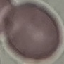
result: negative for malaria parasites
stain: Giemsa
capture: smartphone through the microscope eyepiece
preparation: thin blood smear
image_type: cell patch, automatically extracted from a larger field of view and resized to 64 × 64 pixels